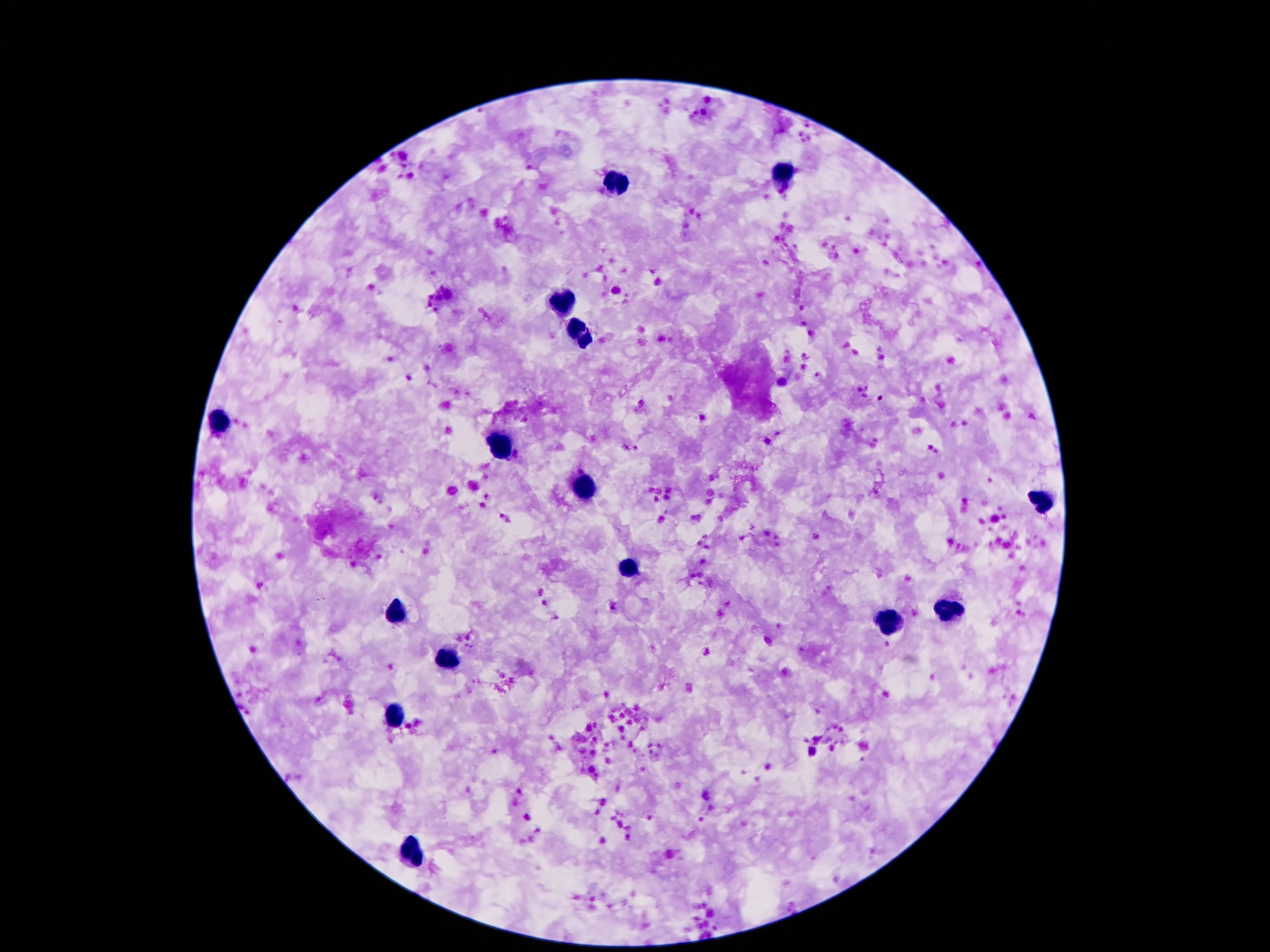

{
  "image_size": "1270×952 pixels",
  "field_of_view": "one from this slide",
  "preparation": "thick blood smear",
  "patient_malaria_status": "not infected",
  "magnification": "100x",
  "leukocyte_locations": "approximate centers as {x, y} in pixels: {780, 172}, {618, 181}, {564, 301}, {579, 334}, {216, 423}, {501, 449}, {581, 484}, {1041, 500}, {629, 569}, {944, 609}, {396, 613}, {889, 624}, {446, 662}, {394, 716}, {417, 853}",
  "stain": "Giemsa",
  "capture": "smartphone camera through the microscope eyepiece"
}